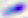
Micrograph. Toxoplasma gondii is shown. 400x magnification.